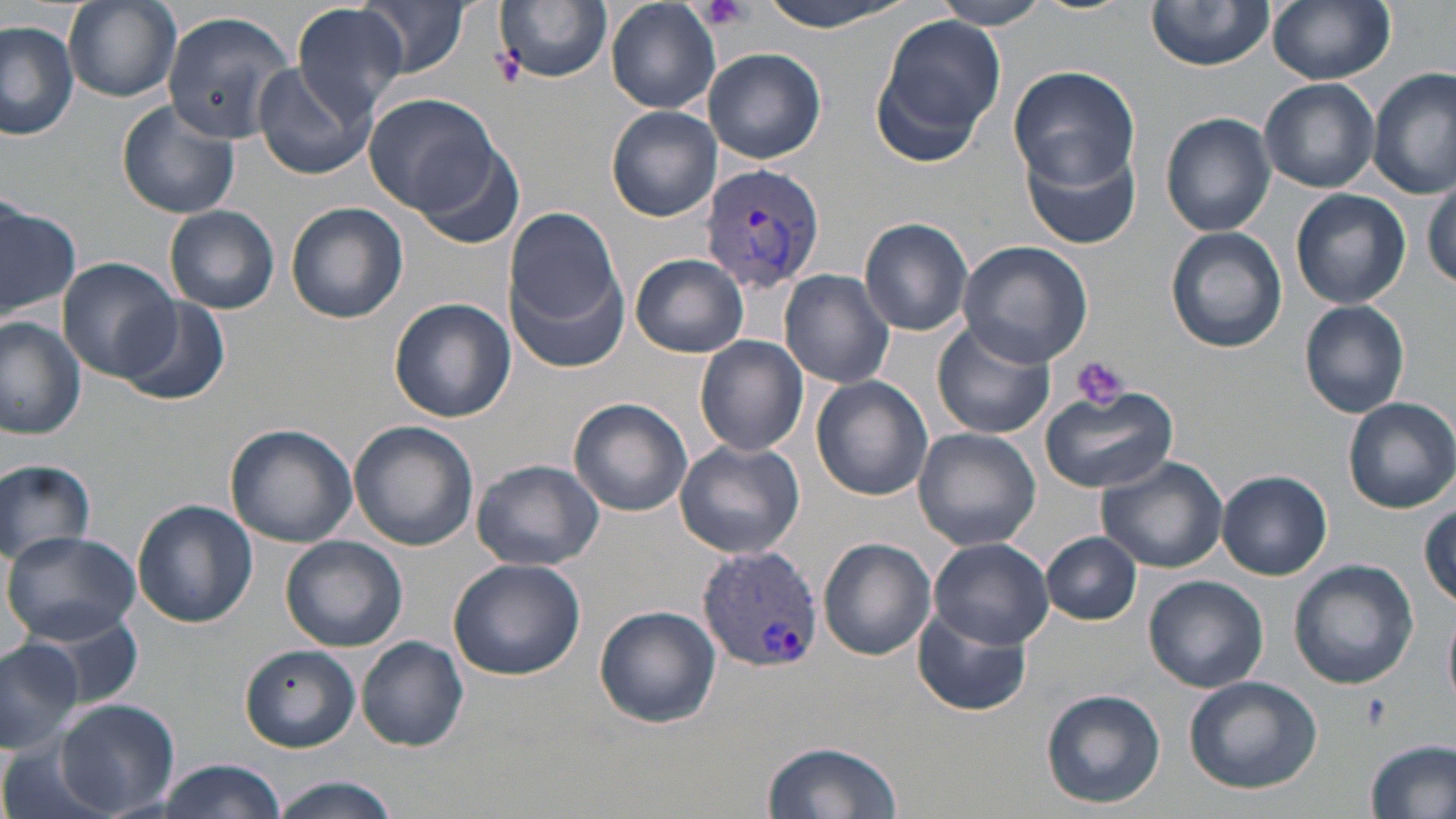

Summary:
  - Coordinate format: approximate bounding boxes as named x1/y1/x2/y2 corners in pixels
  - Platelet locations: (x1=700, y1=0, x2=752, y2=31), (x1=1072, y1=356, x2=1132, y2=411), (x1=1362, y1=693, x2=1388, y2=728)
  - Uninfected red blood cell locations: (x1=493, y1=0, x2=612, y2=86), (x1=754, y1=0, x2=916, y2=32), (x1=933, y1=0, x2=1053, y2=29), (x1=1028, y1=0, x2=1133, y2=15), (x1=1267, y1=0, x2=1394, y2=86), (x1=63, y1=1, x2=181, y2=102), (x1=356, y1=1, x2=469, y2=79), (x1=605, y1=1, x2=720, y2=113), (x1=1146, y1=1, x2=1274, y2=71), (x1=292, y1=4, x2=407, y2=119), (x1=159, y1=8, x2=293, y2=141), (x1=0, y1=9, x2=161, y2=125), (x1=870, y1=14, x2=1009, y2=156), (x1=0, y1=21, x2=79, y2=140), (x1=702, y1=47, x2=827, y2=165), (x1=253, y1=62, x2=374, y2=180), (x1=1007, y1=67, x2=1140, y2=190), (x1=1369, y1=67, x2=1455, y2=198), (x1=1259, y1=78, x2=1380, y2=195), (x1=362, y1=94, x2=502, y2=217), (x1=116, y1=99, x2=241, y2=220), (x1=605, y1=106, x2=722, y2=222), (x1=1161, y1=113, x2=1276, y2=236), (x1=1022, y1=140, x2=1141, y2=251), (x1=413, y1=146, x2=526, y2=251), (x1=1424, y1=182, x2=1456, y2=291), (x1=1291, y1=189, x2=1412, y2=310), (x1=0, y1=196, x2=78, y2=317), (x1=285, y1=203, x2=407, y2=325), (x1=164, y1=205, x2=279, y2=315), (x1=507, y1=211, x2=626, y2=333), (x1=859, y1=217, x2=974, y2=336), (x1=1165, y1=226, x2=1285, y2=354), (x1=957, y1=240, x2=1093, y2=367), (x1=631, y1=254, x2=748, y2=358), (x1=57, y1=258, x2=180, y2=384), (x1=507, y1=259, x2=629, y2=376), (x1=779, y1=268, x2=895, y2=390), (x1=112, y1=297, x2=229, y2=407), (x1=388, y1=298, x2=514, y2=424), (x1=1299, y1=300, x2=1411, y2=418), (x1=1, y1=317, x2=86, y2=442), (x1=931, y1=319, x2=1054, y2=440), (x1=694, y1=336, x2=807, y2=457), (x1=809, y1=375, x2=933, y2=501), (x1=1040, y1=386, x2=1180, y2=492), (x1=1341, y1=396, x2=1454, y2=514), (x1=568, y1=398, x2=693, y2=516), (x1=349, y1=421, x2=478, y2=552), (x1=226, y1=424, x2=358, y2=547), (x1=911, y1=428, x2=1041, y2=552), (x1=673, y1=437, x2=805, y2=560), (x1=1095, y1=455, x2=1228, y2=574), (x1=0, y1=459, x2=96, y2=563), (x1=469, y1=459, x2=605, y2=570), (x1=1216, y1=469, x2=1332, y2=580), (x1=132, y1=500, x2=256, y2=627), (x1=1418, y1=500, x2=1455, y2=609), (x1=2, y1=529, x2=141, y2=641), (x1=1043, y1=532, x2=1140, y2=626), (x1=281, y1=535, x2=407, y2=651), (x1=817, y1=537, x2=937, y2=660), (x1=927, y1=538, x2=1055, y2=649), (x1=448, y1=555, x2=587, y2=681), (x1=1288, y1=559, x2=1420, y2=690), (x1=1143, y1=575, x2=1269, y2=693), (x1=593, y1=604, x2=722, y2=728), (x1=18, y1=605, x2=144, y2=714), (x1=914, y1=606, x2=1034, y2=718), (x1=1444, y1=612, x2=1456, y2=709), (x1=0, y1=635, x2=82, y2=754), (x1=357, y1=636, x2=470, y2=752), (x1=239, y1=645, x2=360, y2=753), (x1=1183, y1=675, x2=1322, y2=794), (x1=1039, y1=688, x2=1166, y2=810), (x1=55, y1=699, x2=179, y2=819), (x1=0, y1=734, x2=119, y2=819), (x1=761, y1=738, x2=902, y2=819), (x1=1364, y1=739, x2=1456, y2=819), (x1=148, y1=761, x2=288, y2=819), (x1=265, y1=776, x2=402, y2=818)
  - Plasmodium vivax-infected red blood cell locations: (x1=699, y1=163, x2=825, y2=293), (x1=693, y1=543, x2=824, y2=675)
  - Slide-level diagnosis: Plasmodium vivax
  - Image size: 1456×819 pixels
  - Magnification: 1000x
  - Field of view: one of a larger specimen
  - Modality: optical microscopy
  - Stain: May-Grünwald-Giemsa
  - Preparation: thin blood smear